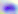

Summary:
  - Identification: Toxoplasma gondii
  - Magnification: 400x
  - Modality: photomicrograph